Classify this cell by malaria status.
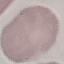
Uninfected.

Cell patch, automatically extracted from a larger field of view and resized to 64 × 64 pixels. Giemsa stain. Thin blood film. Acquired by smartphone through the microscope eyepiece.